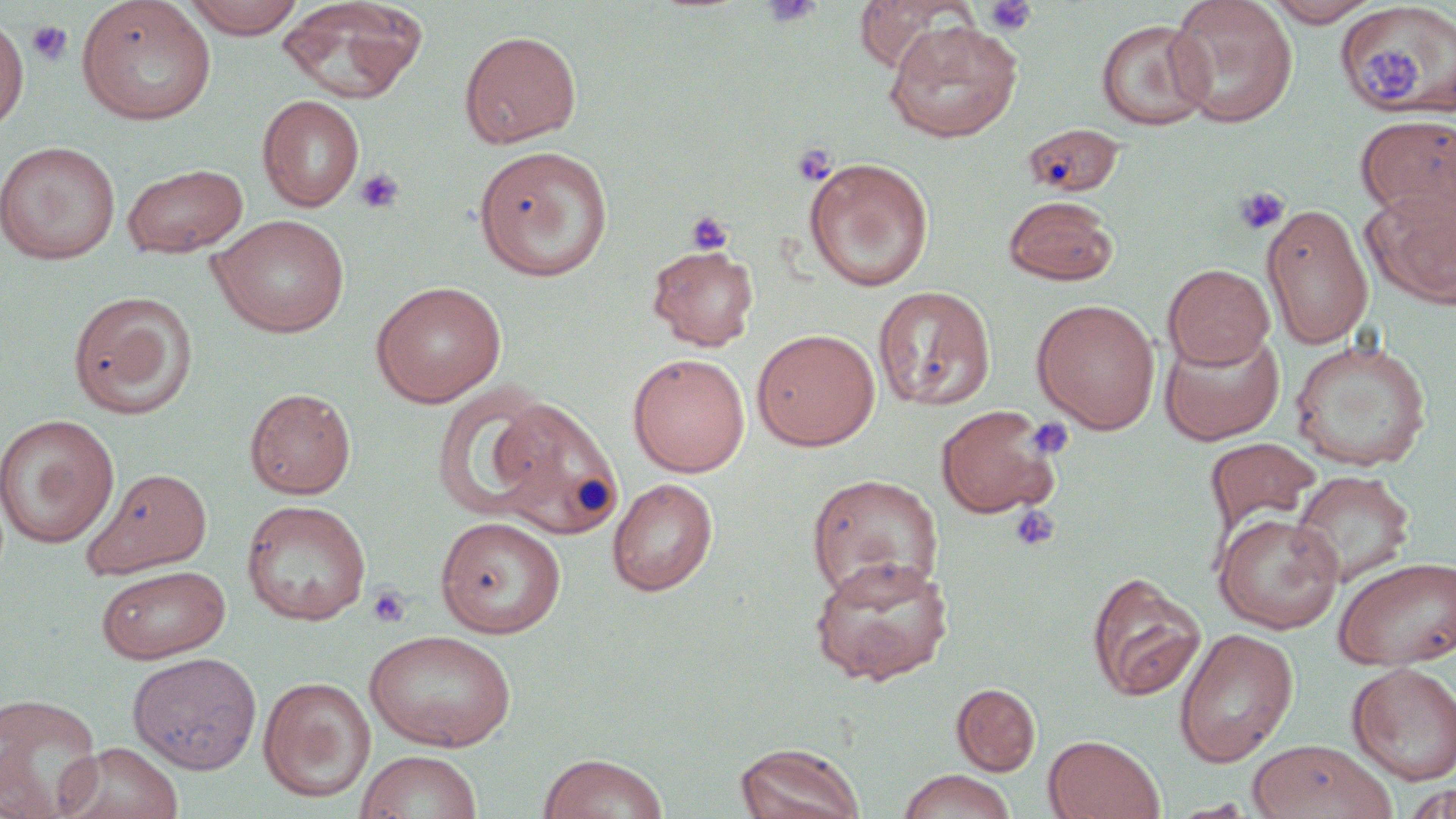

Approximate bounding boxes as named x1/y1/x2/y2 corners in pixels. Platelet locations: (x1=761, y1=0, x2=823, y2=28), (x1=983, y1=0, x2=1038, y2=36), (x1=26, y1=21, x2=73, y2=67), (x1=1361, y1=48, x2=1430, y2=103), (x1=792, y1=143, x2=836, y2=186), (x1=355, y1=168, x2=404, y2=214), (x1=1233, y1=185, x2=1289, y2=235), (x1=685, y1=210, x2=734, y2=255), (x1=1027, y1=416, x2=1074, y2=460), (x1=1010, y1=504, x2=1060, y2=552), (x1=367, y1=584, x2=412, y2=628). Uninfected red blood cell locations (subset): (x1=76, y1=0, x2=217, y2=125), (x1=180, y1=0, x2=307, y2=38), (x1=275, y1=0, x2=429, y2=104), (x1=851, y1=0, x2=981, y2=73), (x1=1165, y1=0, x2=1299, y2=127), (x1=1261, y1=0, x2=1382, y2=26), (x1=0, y1=15, x2=29, y2=132), (x1=1096, y1=18, x2=1213, y2=130), (x1=883, y1=19, x2=1024, y2=144), (x1=459, y1=29, x2=583, y2=148), (x1=257, y1=94, x2=365, y2=212), (x1=1356, y1=113, x2=1455, y2=224), (x1=1025, y1=124, x2=1124, y2=198), (x1=0, y1=140, x2=121, y2=265), (x1=473, y1=145, x2=614, y2=282), (x1=803, y1=157, x2=934, y2=292), (x1=121, y1=162, x2=249, y2=258), (x1=1362, y1=187, x2=1456, y2=308), (x1=1004, y1=195, x2=1119, y2=285), (x1=1261, y1=202, x2=1373, y2=350), (x1=209, y1=214, x2=350, y2=338), (x1=647, y1=244, x2=760, y2=351), (x1=1163, y1=263, x2=1274, y2=369), (x1=371, y1=280, x2=507, y2=407), (x1=872, y1=285, x2=996, y2=411), (x1=67, y1=290, x2=199, y2=420), (x1=1032, y1=298, x2=1161, y2=434), (x1=752, y1=328, x2=880, y2=451), (x1=1158, y1=328, x2=1285, y2=445), (x1=1289, y1=338, x2=1432, y2=471), (x1=628, y1=353, x2=750, y2=477), (x1=431, y1=384, x2=559, y2=523), (x1=245, y1=387, x2=356, y2=499), (x1=488, y1=395, x2=625, y2=540), (x1=934, y1=403, x2=1064, y2=519), (x1=0, y1=413, x2=119, y2=548), (x1=1203, y1=436, x2=1323, y2=545), (x1=83, y1=467, x2=213, y2=578), (x1=1290, y1=470, x2=1415, y2=588), (x1=807, y1=473, x2=943, y2=601), (x1=607, y1=477, x2=718, y2=597), (x1=241, y1=499, x2=372, y2=626), (x1=1213, y1=512, x2=1343, y2=633), (x1=434, y1=516, x2=567, y2=638), (x1=808, y1=554, x2=955, y2=686), (x1=1333, y1=556, x2=1456, y2=670), (x1=96, y1=564, x2=231, y2=663), (x1=1086, y1=570, x2=1207, y2=702), (x1=1174, y1=628, x2=1299, y2=767), (x1=363, y1=629, x2=516, y2=752), (x1=127, y1=651, x2=262, y2=774), (x1=1347, y1=661, x2=1456, y2=785), (x1=258, y1=676, x2=376, y2=802), (x1=951, y1=683, x2=1040, y2=776), (x1=0, y1=693, x2=103, y2=818), (x1=1043, y1=734, x2=1164, y2=818), (x1=1248, y1=738, x2=1397, y2=819), (x1=58, y1=741, x2=184, y2=819), (x1=735, y1=742, x2=866, y2=819), (x1=355, y1=749, x2=483, y2=819), (x1=538, y1=752, x2=668, y2=819), (x1=897, y1=769, x2=1017, y2=819), (x1=1400, y1=784, x2=1456, y2=817). Slide-level diagnosis: no evidence of blood parasites. Thin blood smear. May-Grünwald-Giemsa-stained preparation. Optical microscopy. Single field of view. Image is 1456×819 pixels. Captured at 1000x magnification.